Give the position of every malaria parasite.
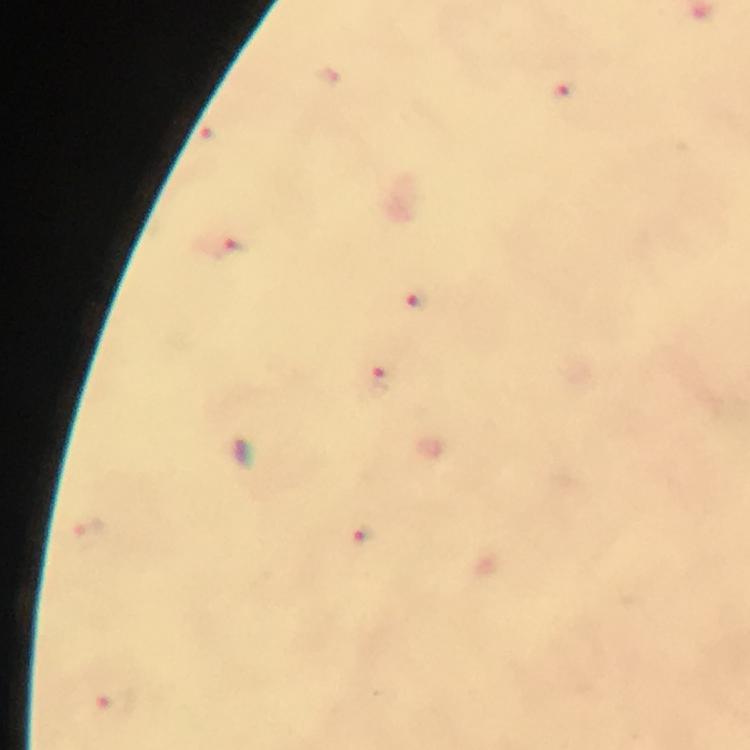

Approximate object centers, in pixels from the top-left corner.
Malaria parasites: (x=561, y=91), (x=227, y=248), (x=416, y=301), (x=381, y=380), (x=359, y=544), (x=116, y=701).

magnification = 100x
capture = smartphone camera through the microscope
context = from a diagnostic examination for malaria
preparation = thick blood smear
stain = Giemsa
immersion oil = applied
cropped from = one field of view
image size = 750×750 pixels